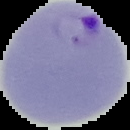 Result: malaria parasites detected. Image is 130×130 pixels. From a thin blood smear. Segmented cell region on a black background.